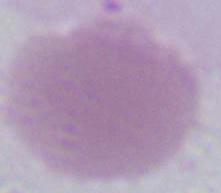
Summary:
  - Modality: micrograph
  - Identification: red blood cell
  - Magnification: 1000x